Point out leukocytes.
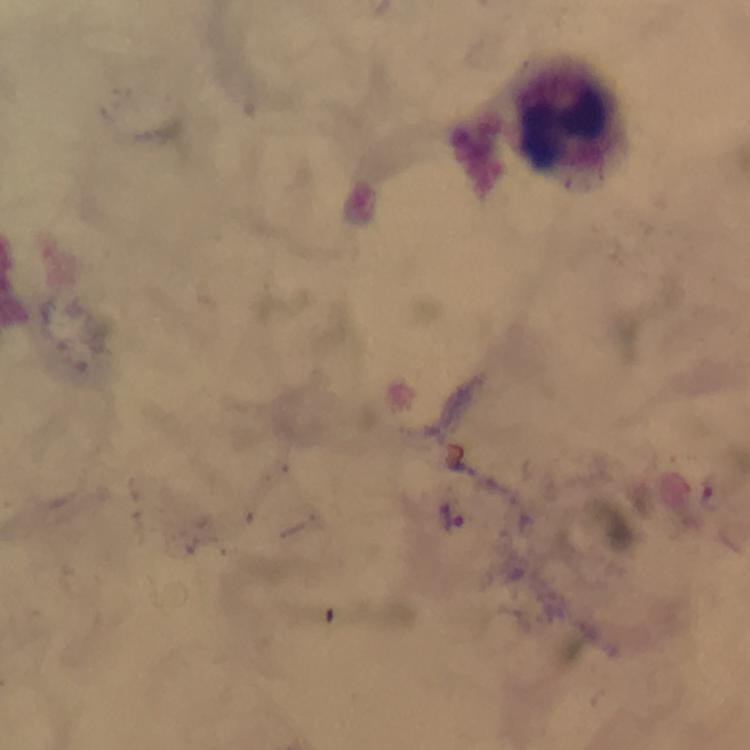

Approximate centers as {x, y} in pixels.
Leukocytes: {566, 119}.

magnification = 100x
image size = 750×750 pixels
Plasmodium parasite locations = approximate centers as {x, y} in pixels: {452, 516}
preparation = thick smear
cropped from = one field of view
stain = Giemsa
capture = smartphone mounted on the microscope
context = from a diagnostic examination for malaria
immersion oil = applied